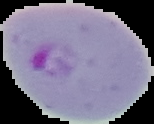
Image is 154×124 pixels. Malaria status: parasitized. The area outside the segmented cell region is set to black. From a thin blood film.